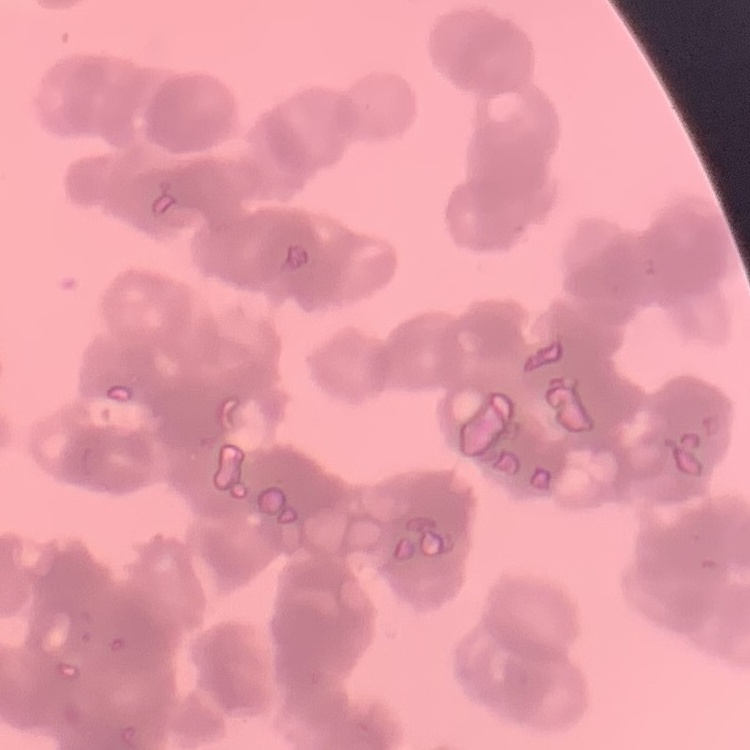

red blood cell morphology = rouleaux formation
preparation = thin blood smear
image type = one tile cut from a larger photomicrograph
stain = Field's or Giemsa